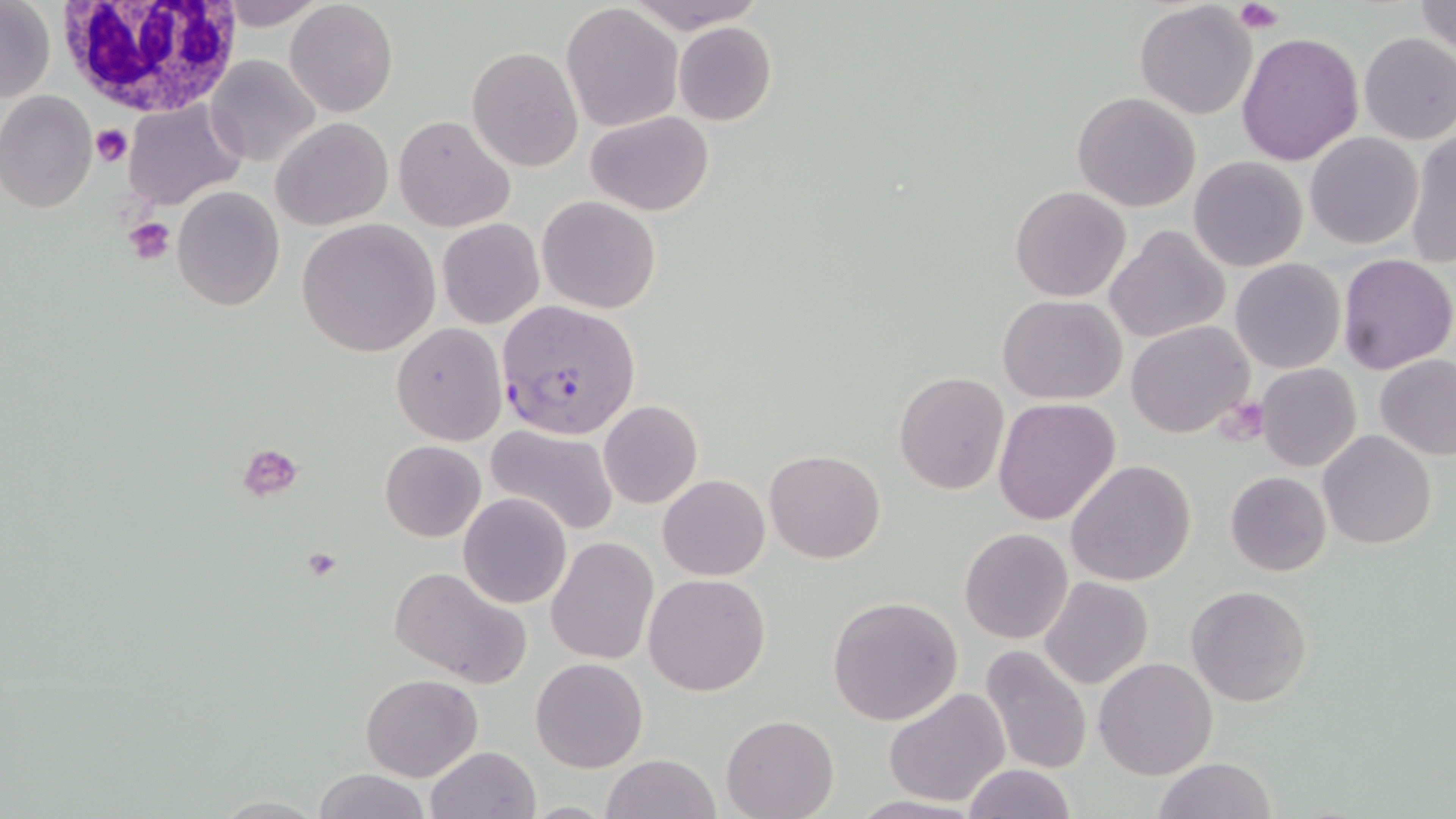

slide-level diagnosis = Plasmodium falciparum
image size = 1456×819 pixels
Plasmodium falciparum-infected red blood cell locations = approximate bounding boxes as (x1, y1, x2, y2) in pixels: (496, 303, 640, 439)
field of view = one of a larger specimen
preparation = thin blood smear
stain = May-Grünwald-Giemsa
uninfected red blood cell locations = approximate bounding boxes as (x1, y1, x2, y2) in pixels: (213, 0, 329, 28), (625, 0, 763, 29), (1413, 0, 1456, 57), (0, 1, 55, 104), (285, 1, 398, 118), (1133, 2, 1258, 118), (561, 3, 684, 132), (673, 22, 777, 126), (1237, 30, 1365, 166), (1358, 32, 1456, 144), (467, 45, 582, 173), (207, 55, 319, 166), (0, 91, 97, 213), (1072, 92, 1201, 211), (124, 100, 247, 211), (586, 111, 715, 216), (395, 115, 514, 233), (271, 117, 393, 231), (1406, 127, 1456, 269), (1305, 132, 1424, 249), (1189, 156, 1308, 272), (1009, 185, 1131, 303), (171, 186, 285, 312), (538, 196, 660, 314), (437, 217, 545, 330), (296, 219, 441, 358), (1105, 225, 1230, 345), (1336, 252, 1456, 375), (1229, 258, 1345, 373), (997, 295, 1129, 403), (1125, 321, 1255, 439), (391, 323, 506, 444), (1375, 355, 1456, 459), (1256, 363, 1362, 472), (893, 372, 1009, 494), (992, 397, 1120, 525), (598, 400, 703, 509), (486, 426, 620, 535), (1318, 430, 1436, 549), (379, 439, 486, 542), (765, 449, 886, 563), (1065, 459, 1198, 587), (1225, 470, 1331, 577), (658, 474, 769, 581), (459, 494, 572, 609), (959, 528, 1072, 644), (546, 536, 660, 665), (388, 565, 533, 687), (644, 572, 769, 695), (1039, 576, 1154, 690), (1186, 584, 1312, 708), (826, 595, 965, 725), (977, 643, 1092, 776), (530, 657, 649, 772), (1094, 657, 1218, 779), (361, 674, 483, 782), (883, 687, 1010, 807), (721, 715, 838, 819), (424, 746, 542, 819), (600, 753, 724, 819), (1153, 757, 1277, 818), (962, 764, 1076, 819), (313, 769, 432, 819)
magnification = 1000x
modality = light microscopy
platelet locations = approximate bounding boxes as (x1, y1, x2, y2) in pixels: (1235, 2, 1283, 33), (92, 125, 132, 168), (123, 213, 176, 264), (1218, 397, 1269, 443), (239, 443, 304, 501), (299, 549, 344, 582)
white blood cell locations = approximate bounding boxes as (x1, y1, x2, y2) in pixels: (55, 0, 245, 118)